Locate and identify every blood parasite.
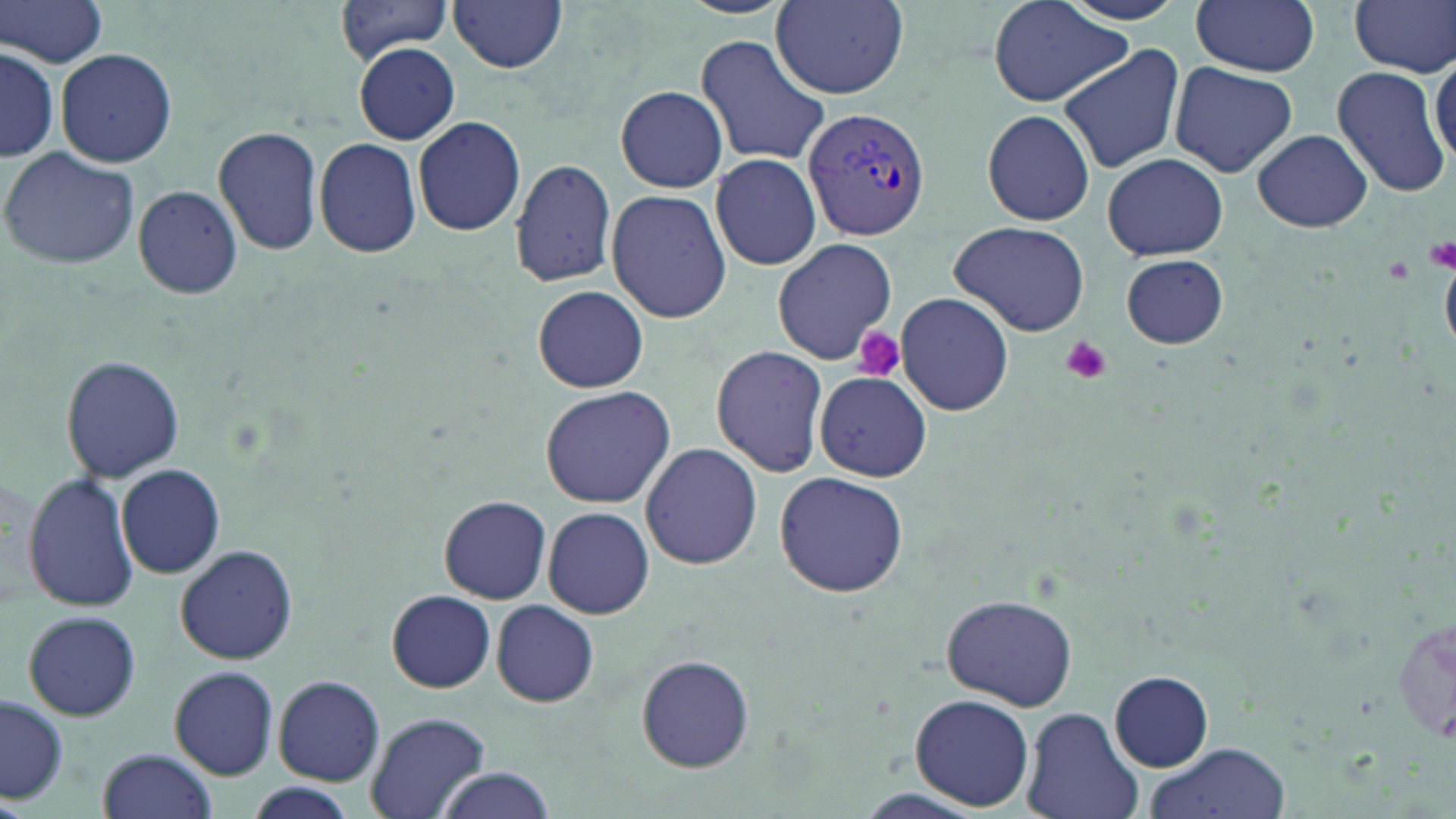

Approximate bounding boxes as [x1, y1, x2, y2] in pixels.
Plasmodium vivax-infected red blood cells: [802, 105, 932, 244].
No Plasmodium falciparum, Plasmodium ovale, Plasmodium malariae, Babesia divergens, or Trypanosoma brucei observed.

slide_level_diagnosis: Plasmodium vivax
platelet_locations: 'approximate bounding boxes as [x1, y1, x2, y2] in pixels: [1423, 237, 1456, 273], [1383, 258, 1414, 284], [854, 328, 905, 382], [1060, 335, 1112, 383]'
magnification: 1000x
uninfected_red_blood_cell_locations: 'approximate bounding boxes as [x1, y1, x2, y2] in pixels: [1, 0, 108, 69], [335, 0, 456, 61], [770, 0, 911, 102], [987, 0, 1131, 107], [1053, 0, 1192, 26], [1190, 0, 1321, 76], [1350, 0, 1455, 77], [450, 1, 568, 73], [696, 34, 832, 170], [353, 43, 459, 144], [2, 46, 58, 160], [1057, 46, 1185, 173], [1430, 47, 1456, 170], [56, 48, 178, 168], [1168, 61, 1298, 179], [1331, 65, 1453, 198], [616, 85, 728, 193], [982, 108, 1096, 226], [413, 116, 526, 237], [214, 126, 324, 255], [1252, 128, 1373, 233], [313, 136, 423, 258], [0, 144, 141, 271], [1102, 152, 1229, 261], [711, 153, 823, 272], [509, 159, 617, 286], [132, 184, 243, 300], [605, 188, 732, 323], [949, 220, 1092, 337], [770, 238, 896, 366], [1119, 253, 1230, 349], [531, 285, 650, 393], [894, 292, 1016, 415], [710, 346, 829, 478], [61, 356, 184, 482], [815, 372, 932, 482], [540, 385, 676, 508], [640, 442, 763, 570], [117, 464, 225, 579], [23, 470, 140, 614], [2, 471, 48, 607], [773, 471, 909, 598], [438, 495, 552, 604], [542, 506, 655, 620], [176, 544, 298, 665], [386, 589, 496, 693], [941, 591, 1079, 711], [493, 600, 597, 708], [1392, 606, 1455, 756], [22, 610, 141, 721], [635, 653, 754, 773], [169, 666, 280, 779], [1111, 671, 1212, 770], [272, 675, 385, 786], [910, 693, 1034, 810], [2, 694, 68, 804], [1021, 707, 1142, 819], [365, 711, 491, 819], [1145, 741, 1291, 819], [98, 747, 216, 818], [427, 767, 557, 819], [240, 785, 362, 817]'
field_of_view: one of a larger specimen
modality: light microscopy
preparation: thin blood film
image_size: 1456×819 pixels
stain: May-Grünwald-Giemsa